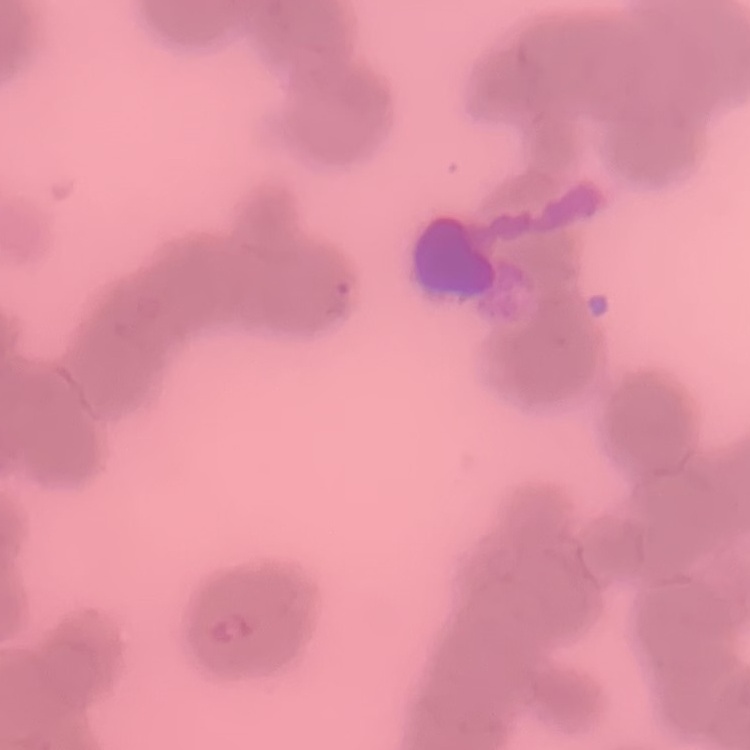
Summary:
  - Erythrocyte morphology: rouleaux formation
  - Image type: square crop of a larger photomicrograph
  - Stain: Field's or Giemsa
  - Preparation: thin blood film